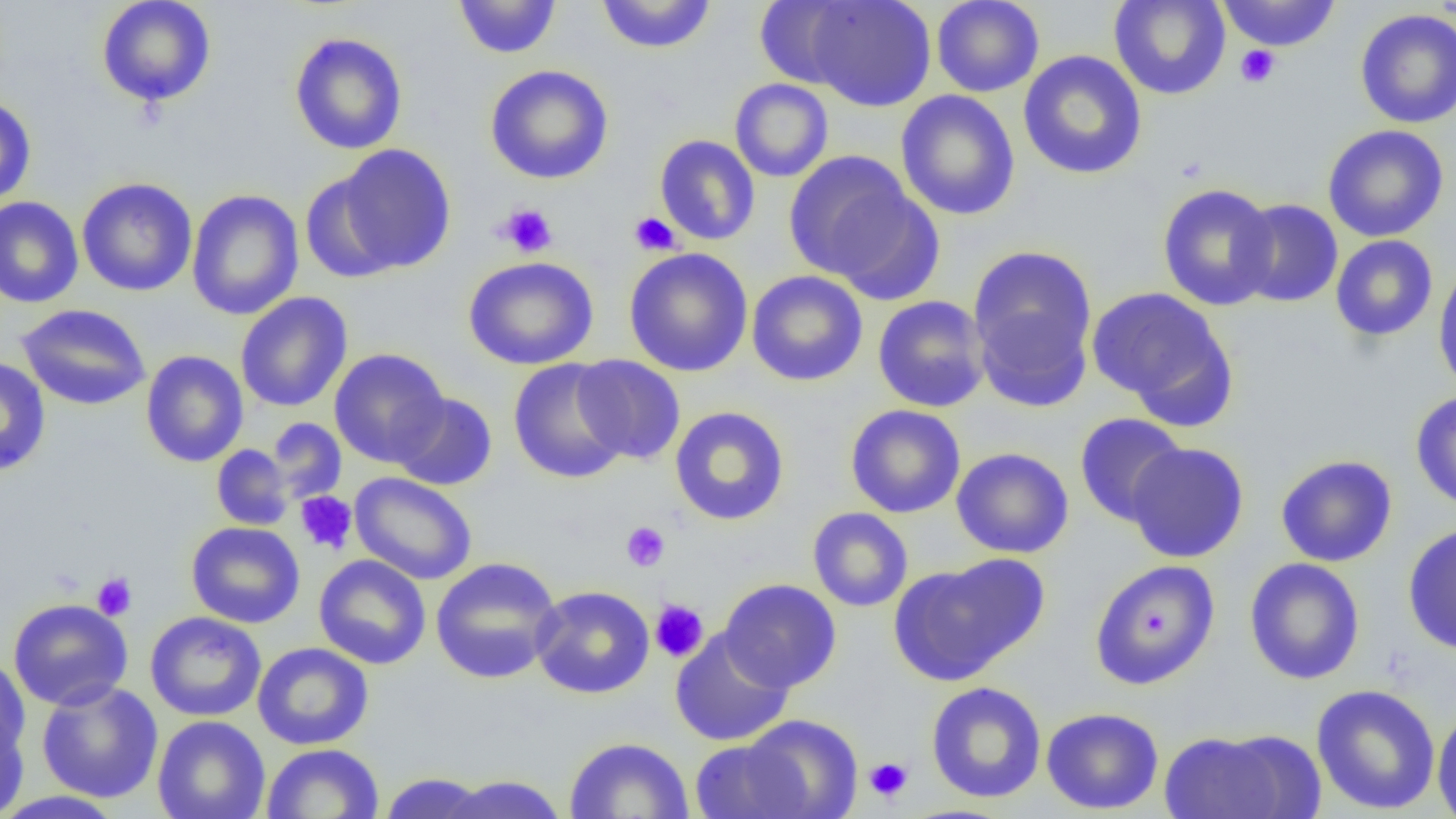
Approximate bounding boxes as [x1, y1, x2, y2] in pixels. Uninfected red blood cell locations: [95, 0, 217, 108], [453, 0, 562, 59], [596, 0, 716, 54], [753, 0, 863, 89], [804, 0, 937, 112], [931, 0, 1045, 98], [1108, 0, 1231, 100], [1217, 0, 1342, 52], [1354, 8, 1456, 128], [289, 32, 408, 155], [1018, 50, 1147, 180], [484, 64, 614, 185], [730, 78, 833, 182], [896, 90, 1020, 221], [0, 95, 36, 207], [1322, 124, 1449, 242], [655, 134, 761, 246], [330, 144, 457, 275], [783, 150, 924, 287], [300, 169, 404, 285], [76, 177, 198, 296], [1157, 183, 1279, 311], [186, 189, 304, 321], [0, 197, 84, 308], [1233, 199, 1343, 307], [1330, 235, 1438, 342], [967, 245, 1098, 408], [623, 247, 754, 377], [463, 255, 599, 370], [1433, 263, 1456, 394], [746, 270, 869, 387], [1087, 286, 1234, 417], [235, 292, 352, 413], [873, 295, 991, 413], [16, 304, 151, 411], [329, 348, 450, 467], [141, 351, 249, 467], [572, 355, 686, 465], [0, 356, 51, 477], [508, 358, 631, 484], [1410, 390, 1456, 512], [391, 392, 497, 491], [846, 404, 966, 518], [669, 406, 790, 525], [1074, 412, 1189, 527], [266, 418, 347, 503], [1124, 441, 1249, 563], [212, 444, 293, 530], [951, 447, 1074, 558], [1275, 454, 1398, 567], [350, 472, 478, 585], [807, 507, 913, 612], [186, 522, 305, 628], [1402, 522, 1456, 655], [314, 554, 431, 669], [429, 556, 563, 685], [1244, 557, 1365, 685], [888, 559, 1039, 685], [1089, 559, 1221, 690], [719, 578, 842, 692], [530, 585, 655, 699], [8, 597, 133, 710], [145, 611, 266, 722], [669, 629, 794, 746], [252, 642, 374, 750], [0, 654, 31, 767], [36, 680, 163, 803], [925, 681, 1047, 803], [1311, 683, 1441, 815], [1040, 707, 1164, 814], [1432, 707, 1456, 819], [740, 714, 863, 818], [0, 715, 29, 818], [152, 715, 270, 819], [1158, 727, 1312, 819], [563, 736, 695, 819], [689, 739, 810, 819], [261, 743, 384, 819], [377, 772, 493, 818], [438, 775, 569, 819], [0, 790, 125, 818]. Platelet locations: [1235, 45, 1280, 88], [498, 203, 558, 258], [629, 212, 681, 256], [295, 491, 358, 555], [621, 521, 670, 572], [91, 572, 137, 620], [649, 598, 709, 663], [864, 757, 913, 802]. Slide-level diagnosis: no evidence of blood parasites. Image is 1456×819 pixels. Single field of view. Thin blood smear. Optical microscopy. Captured at 1000x magnification.